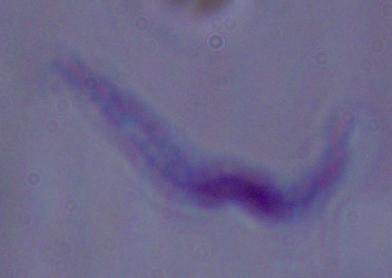

Summary:
  - Identification: trypanosome
  - Modality: micrograph
  - Magnification: 1000x